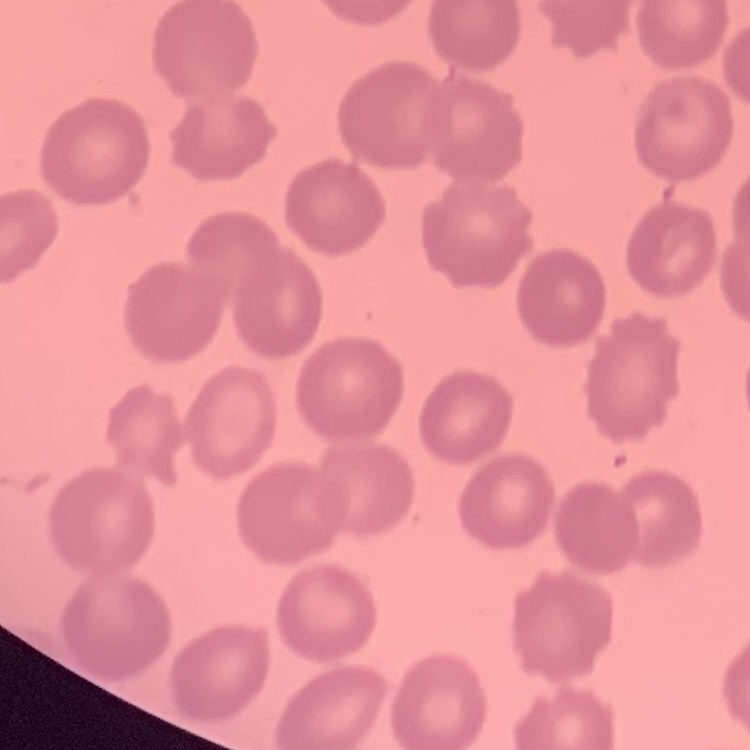

The red blood cells exhibit no rouleaux formation. Stained with either Field's or Giemsa. Thin blood film. Square crop of a larger photomicrograph.